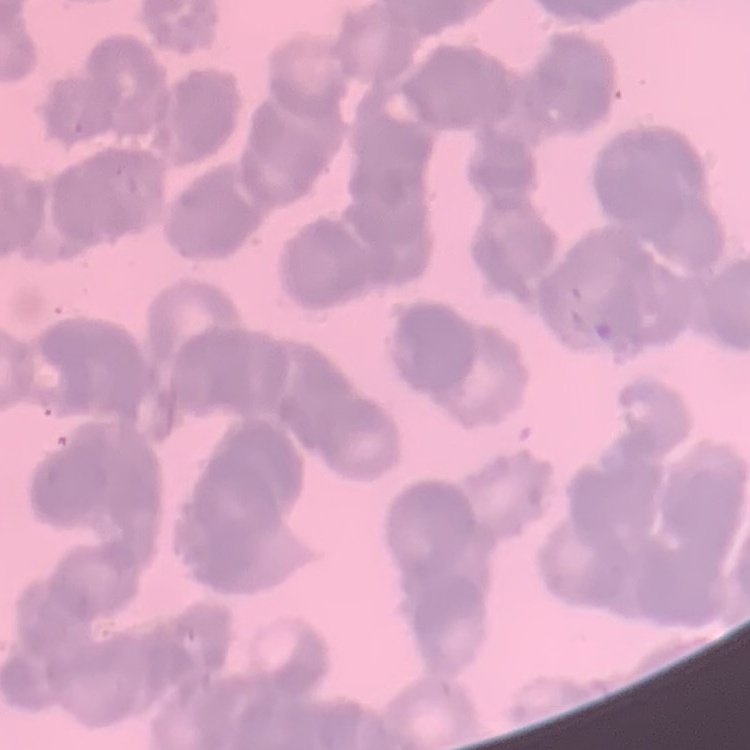 The erythrocytes show rouleaux formation. Stained with either Field's or Giemsa. Thin blood film. One tile cut from a larger photomicrograph.